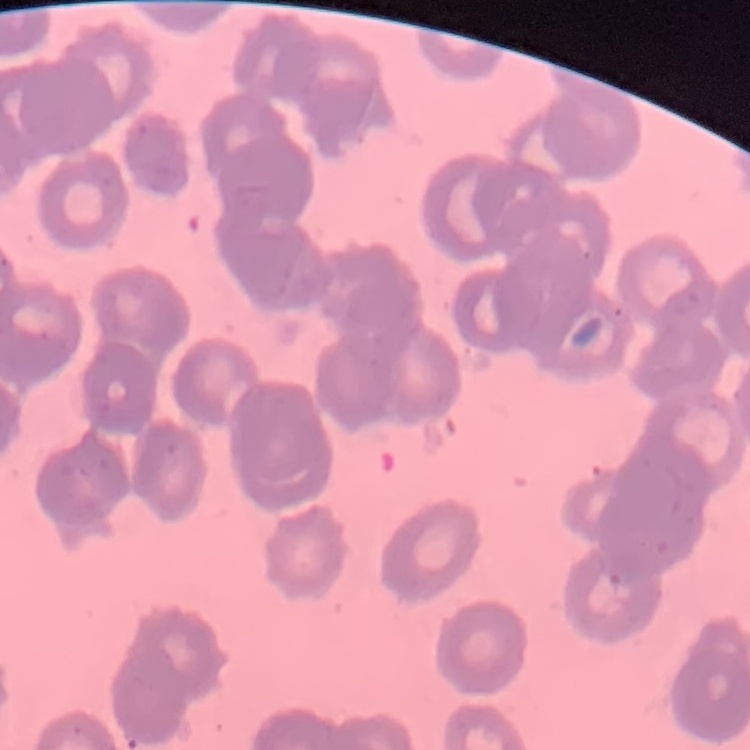

{
  "erythrocyte_morphology": "rouleaux formation",
  "image_type": "square crop of a larger photomicrograph",
  "preparation": "thin blood smear",
  "stain": "Field's or Giemsa"
}